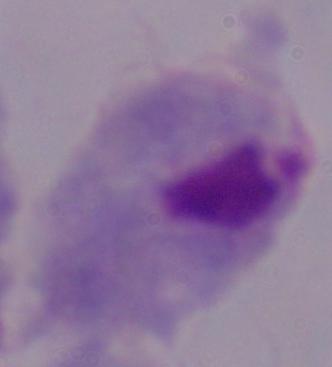
A trichomonad is shown. Captured at 1000x magnification. Photomicrograph.